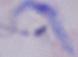

{
  "magnification": "1000x",
  "identification": "trypanosome",
  "modality": "micrograph"
}